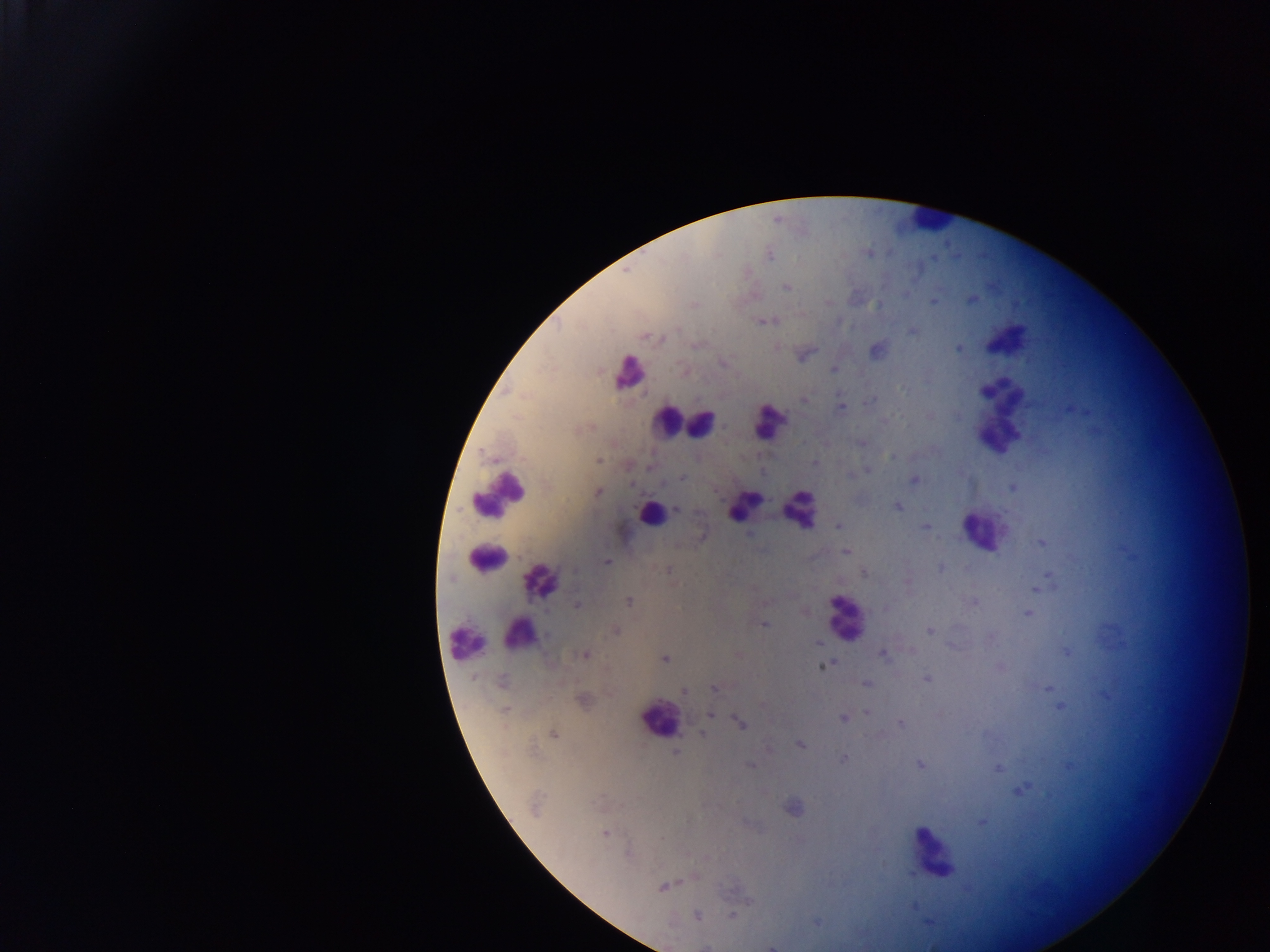
Approximate centers as x y in pixels.
Summary:
  - Malaria parasite locations: 770 254; 932 258; 786 287; 972 300; 932 301; 828 302; 694 304; 771 320; 761 321; 912 332; 645 336; 661 339; 958 349; 876 350; 804 355; 723 363; 834 369; 904 390; 986 391; 804 399; 869 401; 840 408; 1069 410; 930 416; 885 419; 861 443; 891 458; 598 460; 815 462; 650 467; 867 470; 762 473; 850 476; 682 478; 914 479; 632 484; 1012 487; 598 492; 896 506; 677 509; 838 525; 925 526; 1041 543; 846 552; 606 562; 940 568; 668 571; 864 573; 1048 576; 907 582; 1036 589; 628 601; 973 603; 577 606; 885 608; 1027 613; 764 625; 928 630; 615 632; 991 637; 817 642; 951 646; 1066 651; 883 654; 585 655; 665 659; 822 667; 1000 667; 926 678; 502 681; 865 683; 714 688; 1047 689; 684 691; 582 700; 1059 707; 506 708; 866 712; 710 715; 843 718; 740 722; 899 723; 702 733; 553 734; 800 745; 675 752; 843 760; 920 764; 750 765; 1068 766; 997 768; 1021 790; 792 808; 981 822; 604 833; 628 853; 909 874; 663 887; 696 915; 732 915; 816 923; 928 923; 772 947
  - Leukocyte locations: 928 220; 1006 338; 630 374; 998 415; 770 420; 667 421; 700 424; 499 494; 744 504; 799 510; 650 514; 983 531; 485 558; 544 580; 844 613; 518 631; 465 643; 657 720; 932 853
  - Country: Ghana
  - Capture: mobile-phone photograph through a microscope
  - Image size: 1270×952 pixels
  - Field of view: single
  - Preparation: thick blood smear